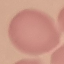

Summary:
  - Result: no malaria parasites detected
  - Preparation: thin blood smear
  - Image type: automatically extracted cell patch, resized to 64 × 64 pixels
  - Capture: smartphone camera at the microscope eyepiece
  - Stain: Giemsa